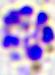

400x magnification. Micrograph. A white blood cell is seen.